Assess this cell for malaria.
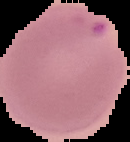

Parasitized.

Summary:
  - Preparation: thin blood smear
  - Image size: 130×142 pixels
  - Image type: segmented cell region with the area outside set to black